Outline each blood parasite and name the species.
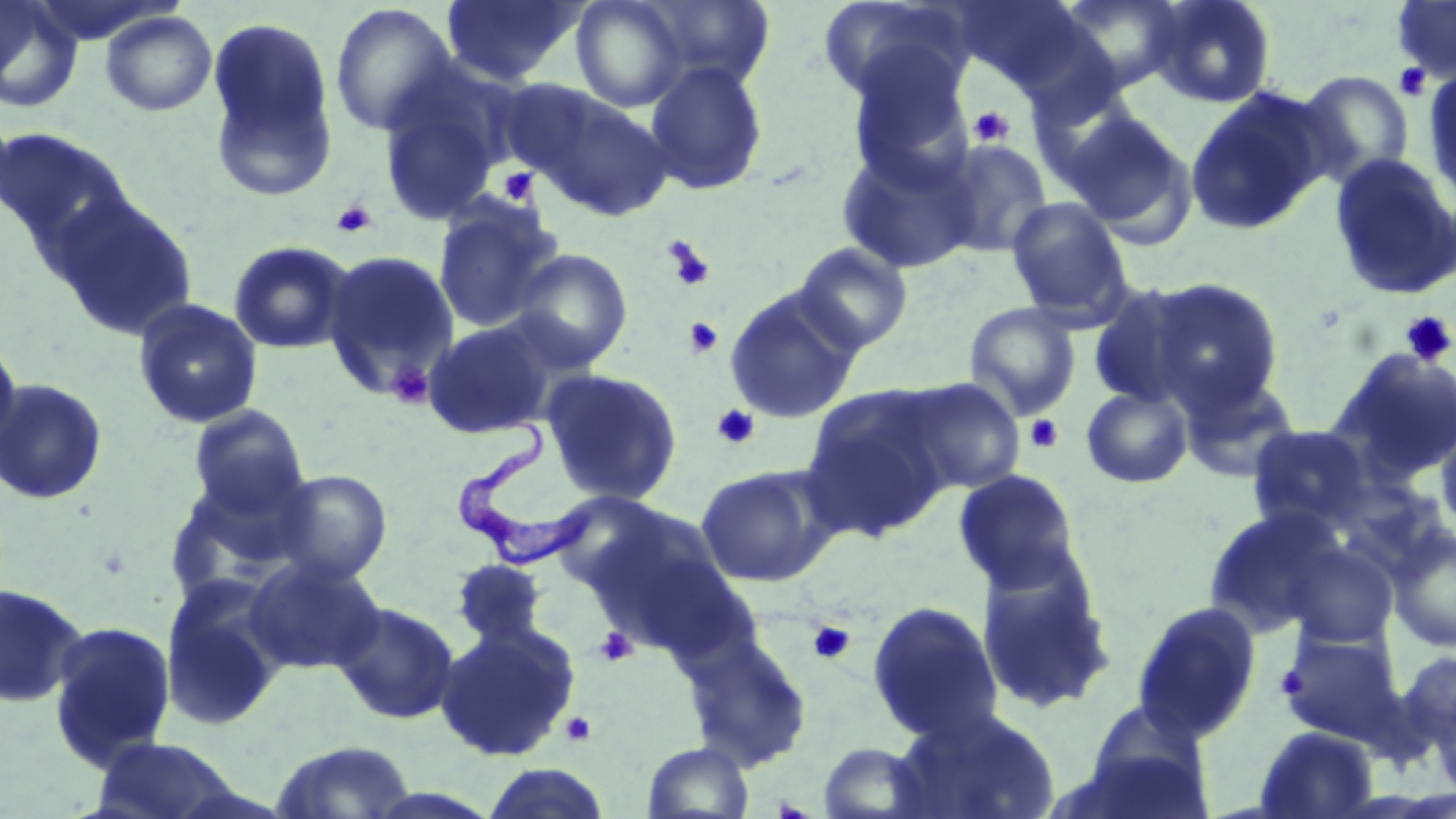
Approximate bounding boxes as (x1,y1)-(x2,y2) corner pairs in pixels.
Trypanosoma brucei: (455,411)-(591,575).
No Plasmodium falciparum, Plasmodium ovale, Plasmodium malariae, Plasmodium vivax, or Babesia divergens observed.

slide-level diagnosis = Trypanosoma brucei
platelet locations = approximate bounding boxes as (x1,y1)-(x2,y2) corner pairs in pixels: (1393,63)-(1431,101), (968,106)-(1015,148), (497,167)-(541,206), (330,199)-(377,239), (662,236)-(716,292), (1400,310)-(1456,367), (684,316)-(724,358), (386,363)-(435,409), (712,404)-(761,450), (1024,414)-(1064,455), (808,620)-(855,665), (595,626)-(639,667), (1274,664)-(1308,701), (560,711)-(597,747)
magnification = 1000x
modality = optical microscopy
image size = 1456×819 pixels
stain = May-Grünwald-Giemsa
preparation = thin blood film
field of view = one of a larger specimen
uninfected red blood cell locations = approximate bounding boxes as (x1,y1)-(x2,y2) corner pairs in pixels: (0,0)-(82,112), (440,0)-(589,85), (570,0)-(690,112), (637,0)-(777,93), (1051,0)-(1187,97), (1148,0)-(1277,108), (1391,0)-(1456,82), (817,1)-(972,109), (952,1)-(1089,92), (329,3)-(459,138), (100,10)-(217,116), (204,16)-(339,199), (843,47)-(977,185), (642,61)-(770,195), (375,69)-(511,227), (1423,69)-(1456,209), (1297,70)-(1415,186), (508,81)-(675,221), (1184,87)-(1332,236), (0,105)-(18,224), (1060,107)-(1199,245), (0,126)-(133,262), (935,139)-(1054,259), (836,142)-(980,274), (1328,152)-(1456,301), (50,195)-(199,342), (433,197)-(564,333), (1006,197)-(1133,321), (228,240)-(356,355), (793,242)-(914,354), (508,247)-(633,371), (322,249)-(460,396), (1146,278)-(1285,413), (1086,283)-(1206,409), (723,286)-(865,424), (132,297)-(263,430), (964,302)-(1082,420), (421,317)-(561,440), (0,335)-(23,460), (1329,348)-(1456,483), (540,368)-(683,505), (1178,371)-(1302,483), (897,377)-(1026,496), (0,379)-(108,504), (799,385)-(957,539), (1081,386)-(1193,488), (187,404)-(311,518), (1435,415)-(1456,536), (1245,424)-(1375,534), (695,463)-(838,588), (164,467)-(317,600), (269,468)-(393,586), (952,469)-(1084,594), (579,505)-(740,653), (1202,508)-(1346,637), (1387,524)-(1456,653), (1281,541)-(1399,648), (245,555)-(385,675), (451,558)-(550,648), (975,558)-(1118,715), (159,578)-(287,733), (0,582)-(88,709), (331,600)-(460,725), (866,600)-(1003,743), (1131,601)-(1262,743), (47,619)-(178,772), (435,621)-(581,762), (1276,629)-(1405,745), (682,632)-(813,772), (1399,650)-(1456,751), (1076,701)-(1217,819), (889,705)-(1061,819), (1255,726)-(1379,818), (89,736)-(252,819), (270,740)-(417,818), (643,741)-(753,819), (818,741)-(934,819), (482,764)-(611,819)